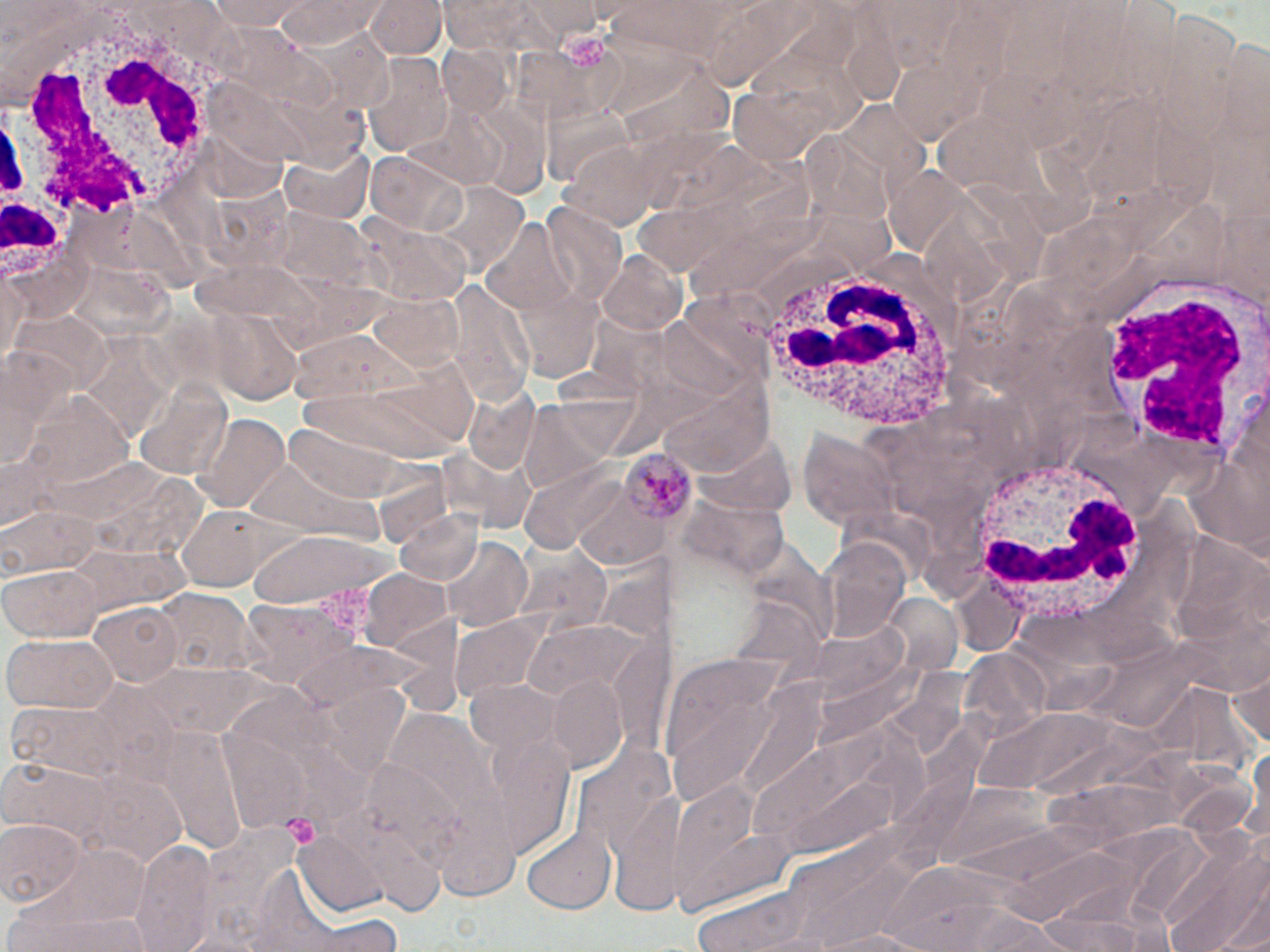

Summary:
  - Coordinate format: approximate bounding boxes as named x1/y1/x2/y2 corners in pixels
  - Platelet locations: (x1=565, y1=36, x2=607, y2=69), (x1=281, y1=814, x2=321, y2=849)
  - Uninfected red blood cell locations: (x1=365, y1=0, x2=444, y2=59), (x1=440, y1=0, x2=537, y2=59), (x1=211, y1=1, x2=315, y2=31), (x1=522, y1=1, x2=608, y2=43), (x1=272, y1=2, x2=384, y2=47), (x1=437, y1=43, x2=512, y2=120), (x1=360, y1=54, x2=454, y2=157), (x1=408, y1=102, x2=504, y2=188), (x1=465, y1=104, x2=551, y2=194), (x1=558, y1=138, x2=667, y2=230), (x1=280, y1=141, x2=375, y2=225), (x1=367, y1=151, x2=470, y2=238), (x1=427, y1=182, x2=528, y2=279), (x1=540, y1=203, x2=625, y2=308), (x1=480, y1=215, x2=582, y2=318), (x1=365, y1=223, x2=472, y2=306), (x1=595, y1=250, x2=689, y2=338), (x1=0, y1=262, x2=27, y2=375), (x1=444, y1=281, x2=535, y2=405), (x1=365, y1=291, x2=465, y2=373), (x1=211, y1=309, x2=307, y2=405), (x1=662, y1=369, x2=773, y2=476), (x1=129, y1=373, x2=231, y2=482), (x1=462, y1=387, x2=539, y2=474), (x1=196, y1=414, x2=289, y2=512), (x1=800, y1=428, x2=899, y2=529), (x1=438, y1=447, x2=532, y2=531), (x1=568, y1=472, x2=674, y2=568), (x1=170, y1=502, x2=282, y2=592), (x1=3, y1=506, x2=100, y2=581), (x1=392, y1=509, x2=485, y2=589), (x1=246, y1=530, x2=399, y2=608), (x1=820, y1=535, x2=908, y2=642), (x1=440, y1=538, x2=531, y2=631), (x1=516, y1=547, x2=608, y2=639), (x1=0, y1=563, x2=105, y2=641), (x1=358, y1=569, x2=454, y2=655), (x1=153, y1=589, x2=252, y2=678), (x1=235, y1=599, x2=358, y2=693), (x1=88, y1=602, x2=187, y2=688), (x1=452, y1=614, x2=547, y2=700), (x1=519, y1=614, x2=657, y2=715), (x1=3, y1=636, x2=117, y2=713), (x1=658, y1=651, x2=812, y2=806), (x1=1227, y1=660, x2=1270, y2=756), (x1=547, y1=674, x2=630, y2=770), (x1=9, y1=700, x2=129, y2=781), (x1=479, y1=721, x2=579, y2=856), (x1=0, y1=762, x2=109, y2=841), (x1=72, y1=770, x2=189, y2=864), (x1=609, y1=789, x2=687, y2=912), (x1=0, y1=819, x2=84, y2=908), (x1=521, y1=823, x2=616, y2=911), (x1=294, y1=828, x2=391, y2=915), (x1=133, y1=840, x2=216, y2=952), (x1=1160, y1=840, x2=1269, y2=950), (x1=9, y1=905, x2=151, y2=952), (x1=1038, y1=909, x2=1170, y2=952), (x1=302, y1=914, x2=404, y2=951), (x1=814, y1=928, x2=926, y2=951)
  - Plasmodium malariae-infected red blood cell locations: (x1=618, y1=448, x2=696, y2=522)
  - White blood cell locations: (x1=33, y1=0, x2=246, y2=224), (x1=3, y1=94, x2=79, y2=289), (x1=743, y1=247, x2=976, y2=434), (x1=1091, y1=266, x2=1270, y2=471), (x1=967, y1=457, x2=1141, y2=629)
  - Slide-level diagnosis: Plasmodium malariae
  - Magnification: 1000x
  - Image size: 1270×952 pixels
  - Preparation: thin blood film
  - Field of view: one of a larger specimen
  - Stain: May-Grünwald-Giemsa
  - Modality: light microscopy